Report the malaria status of this cell.
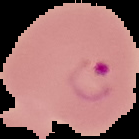
It is parasitized.

preparation = thin blood film
image size = 139×139 pixels
image type = segmented cell region on a black background